Locate every Plasmodium parasite.
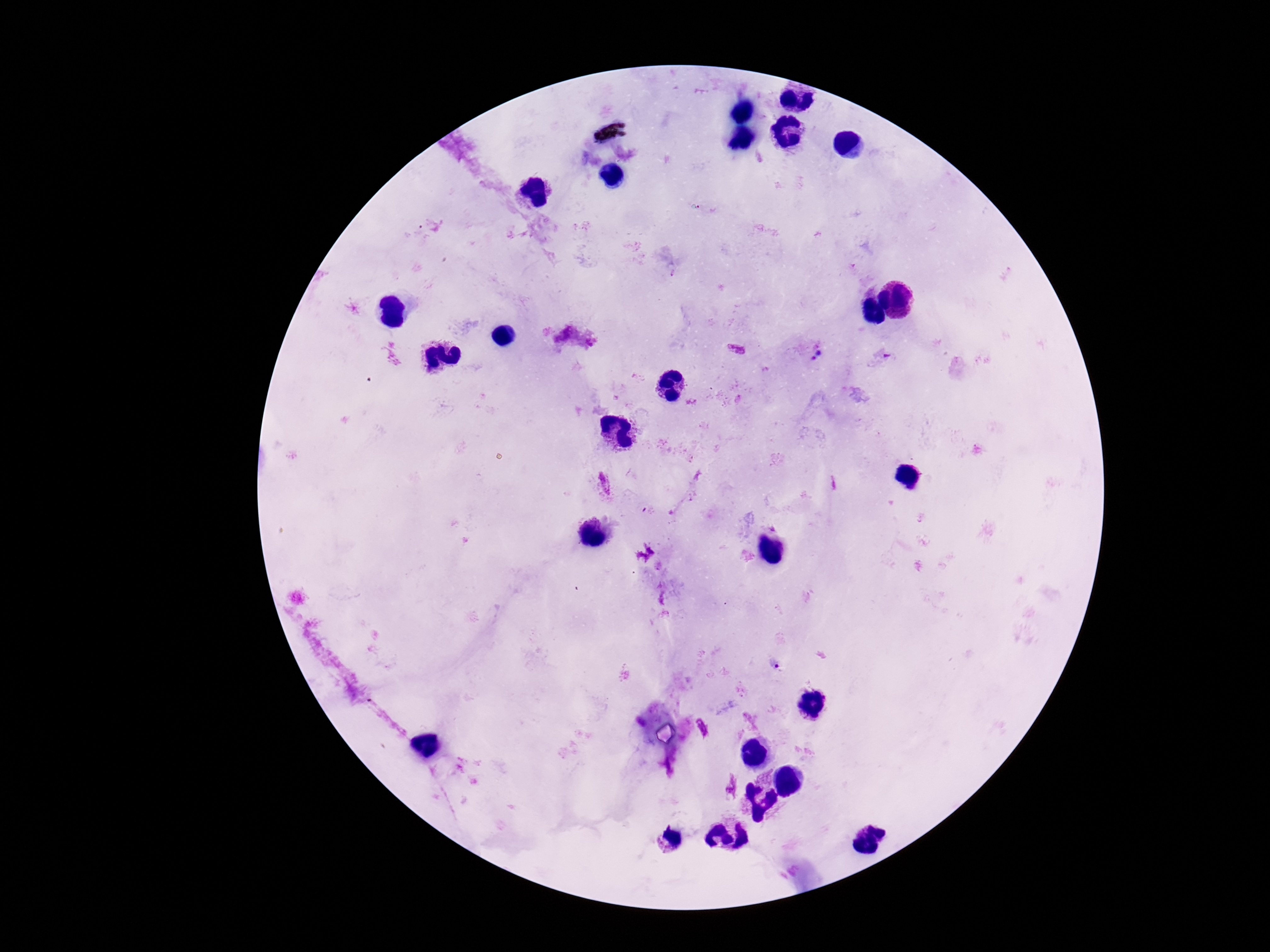

Approximate object centers, in pixels from the top-left corner.
Plasmodium parasites: (x=737, y=348), (x=820, y=353), (x=605, y=484).

Patient malaria status: infected. Single field of view. Photographed through the microscope eyepiece with a smartphone camera. Giemsa-stained preparation. Thick blood film. Image is 1270×952 pixels. 100x magnification.